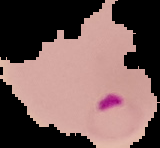

malaria status = parasitized
image type = segmented cell region on a black background
image size = 160×148 pixels
preparation = thin blood film